Locate every malaria parasite and every leukocyte.
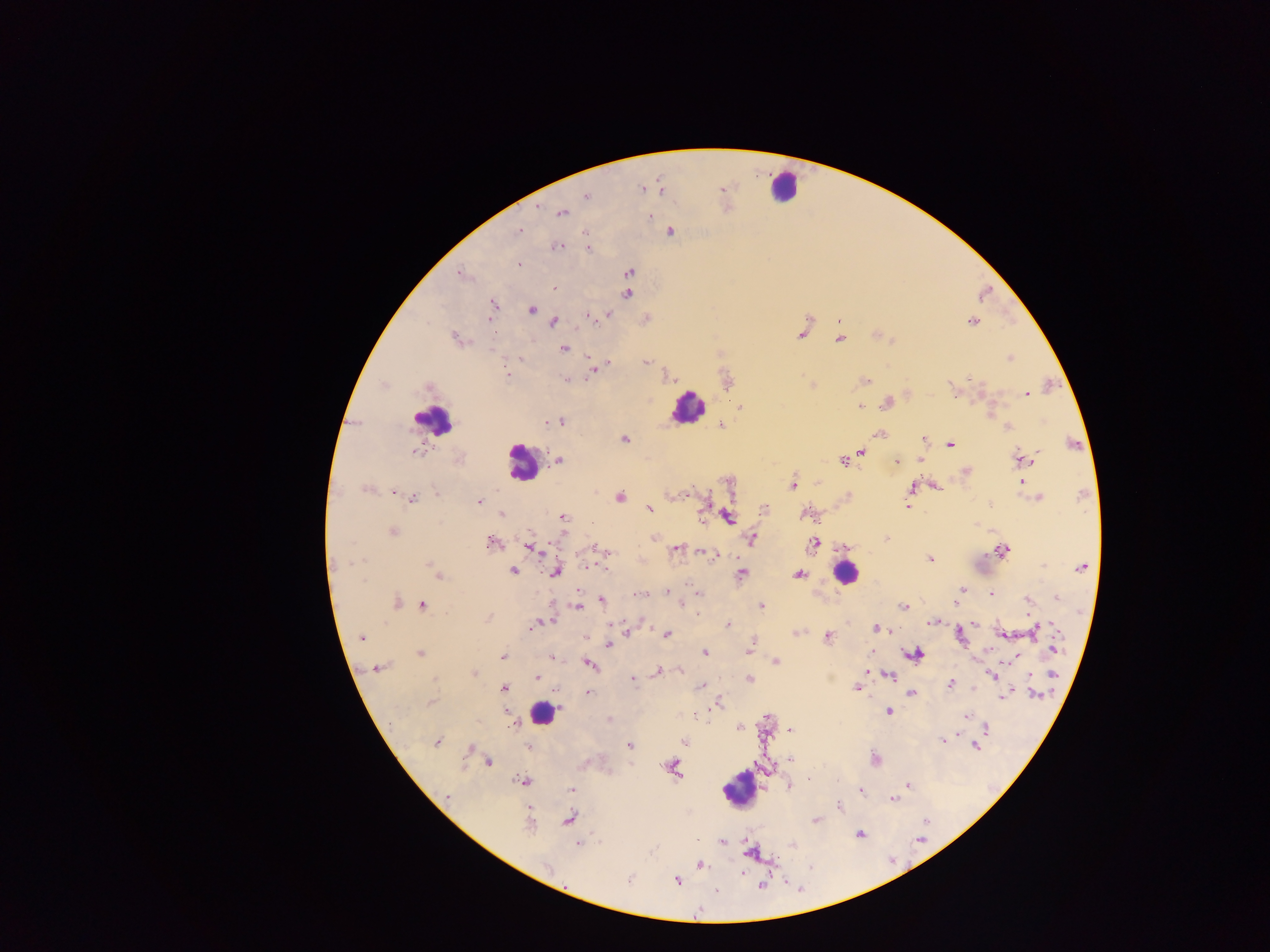
Approximate centers as x y in pixels.
Malaria parasites: 642 189; 586 196; 537 207; 561 213; 650 216; 519 230; 670 231; 585 234; 557 247; 588 248; 518 264; 630 272; 461 274; 553 288; 627 294; 493 305; 531 310; 609 314; 588 316; 490 318; 973 321; 554 322; 801 334; 877 335; 455 337; 839 339; 563 348; 1010 357; 521 358; 608 362; 645 362; 593 370; 508 374; 969 377; 567 380; 865 380; 952 390; 1027 394; 886 403; 859 406; 741 407; 560 421; 549 422; 721 425; 1008 427; 879 434; 922 438; 624 439; 951 445; 416 451; 861 451; 1022 457; 558 460; 919 460; 843 461; 896 461; 967 471; 1021 481; 793 485; 936 486; 912 488; 366 490; 392 493; 437 493; 620 497; 1038 497; 413 498; 479 502; 704 506; 989 506; 907 507; 650 509; 764 510; 501 515; 804 515; 563 517; 727 518; 392 532; 654 538; 886 538; 752 539; 492 542; 813 543; 529 547; 845 547; 676 550; 1002 550; 602 551; 710 555; 930 559; 430 565; 589 566; 1043 566; 1080 567; 606 568; 512 570; 436 571; 556 572; 742 573; 798 574; 438 577; 961 589; 667 591; 992 593; 699 594; 639 595; 1056 597; 958 599; 601 601; 1028 601; 397 602; 955 602; 422 605; 578 606; 682 606; 761 606; 904 606; 487 618; 549 622; 932 622; 974 624; 728 625; 877 628; 530 629; 1036 629; 626 632; 1002 633; 797 634; 666 635; 960 635; 828 636; 361 637; 609 644; 1055 649; 750 650; 420 653; 705 653; 915 654; 502 656; 1015 657; 552 659; 776 662; 589 665; 377 668; 657 671; 680 671; 473 674; 1053 674; 992 675; 889 676; 536 678; 435 680; 633 680; 750 680; 950 684; 702 685; 856 688; 504 689; 588 692; 911 694; 1036 694; 1004 696; 431 702; 718 703; 889 711; 506 712; 965 716; 767 718; 608 719; 512 725; 739 727; 987 728; 792 730; 942 740; 684 742; 437 743; 629 746; 975 746; 529 747; 470 749; 875 759; 791 760; 488 762; 672 767; 809 778; 523 781; 791 784; 907 785; 572 790; 861 792; 447 796; 892 800; 839 806; 568 818; 816 821; 529 823; 859 834; 721 841; 578 844; 750 851; 701 865; 547 867; 630 880; 676 881; 760 885; 717 890.
Leukocytes: 784 185; 686 407; 432 419; 522 463; 845 573; 541 714; 739 789.

Thick blood smear. Sample from Ghana. Mobile-phone photograph taken through the microscope. Image is 1270×952 pixels. One field of view.